Report the malaria status of this cell.
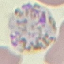
Parasitized.

capture: smartphone through the microscope eyepiece
image_type: automatically extracted cell patch, resized to 64 × 64 pixels
stain: Giemsa
preparation: thin blood film